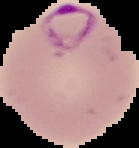
Summary:
  - Image type: cell region segmented out of the field of view; surrounding area masked to black
  - Result: Plasmodium parasites identified
  - Preparation: thin blood film
  - Image size: 139×148 pixels